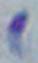
identification = Toxoplasma gondii
modality = micrograph
magnification = 1000x